Report the malaria status of this cell.
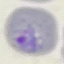
It is parasitized.

{
  "preparation": "thin blood smear",
  "stain": "Giemsa",
  "image_type": "automatically extracted cell patch, resized to 64 × 64 pixels",
  "capture": "smartphone through the microscope eyepiece"
}